Assess the morphology of the red blood cells.
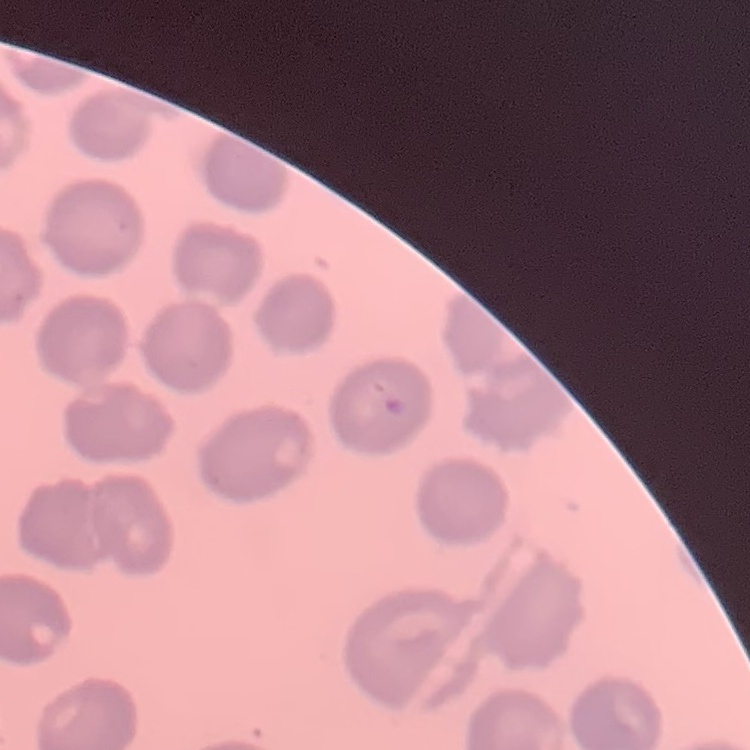

No rouleaux formation.

image type = square crop of a larger photomicrograph
preparation = thin blood film
stain = Field's or Giemsa